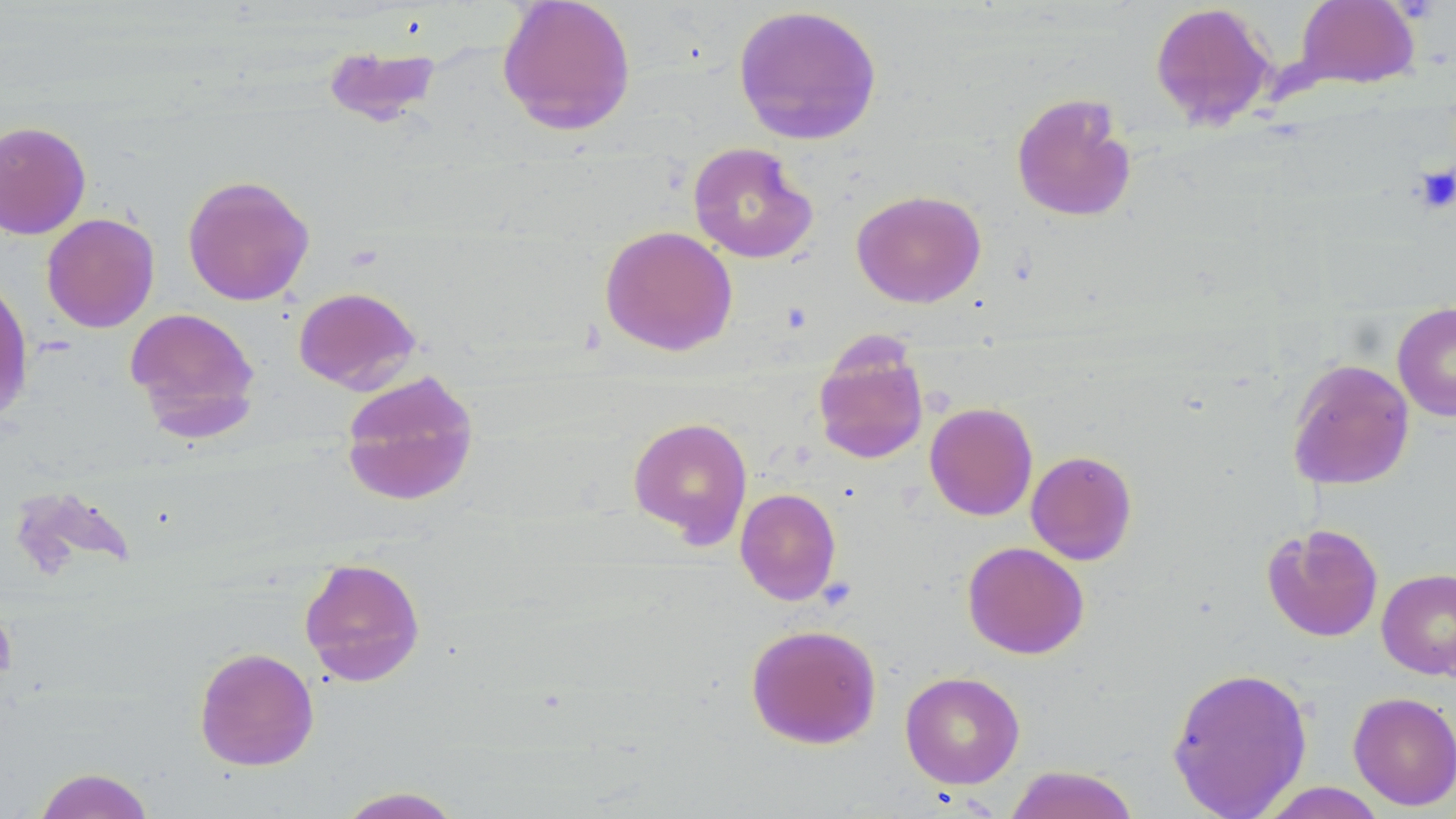 Approximate bounding boxes as (x1,y1)-(x2,y2) corner pairs in pixels. Platelet locations: (1414,164)-(1456,214). Uninfected red blood cell locations: (496,0)-(636,136), (1295,1)-(1419,89), (1149,2)-(1277,130), (731,4)-(884,146), (322,42)-(441,126), (1011,91)-(1138,224), (0,120)-(91,240), (687,142)-(818,263), (182,174)-(315,307), (851,190)-(987,308), (41,213)-(160,333), (599,225)-(738,356), (0,273)-(34,423), (293,286)-(422,393), (1392,302)-(1456,422), (124,307)-(261,439), (812,337)-(930,465), (1286,358)-(1415,490), (339,369)-(479,507), (924,401)-(1038,521), (627,415)-(753,547), (1025,450)-(1138,565), (735,487)-(841,605), (1261,523)-(1384,642), (962,541)-(1089,660), (299,556)-(426,687), (1376,567)-(1456,680), (745,623)-(882,749), (193,646)-(319,771), (1166,665)-(1312,819), (900,671)-(1025,789), (1348,691)-(1456,811), (1005,765)-(1141,819), (33,767)-(156,819), (1255,782)-(1389,818), (334,786)-(466,818). Slide-level diagnosis: negative for blood parasites. Image is 1456×819 pixels. Optical microscopy. Thin blood film. Single field of view. Captured at 1000x magnification. May-Grünwald-Giemsa stain.